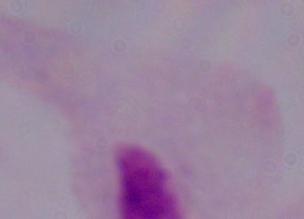

Summary:
  - Magnification: 1000x
  - Modality: micrograph
  - Identification: trichomonad